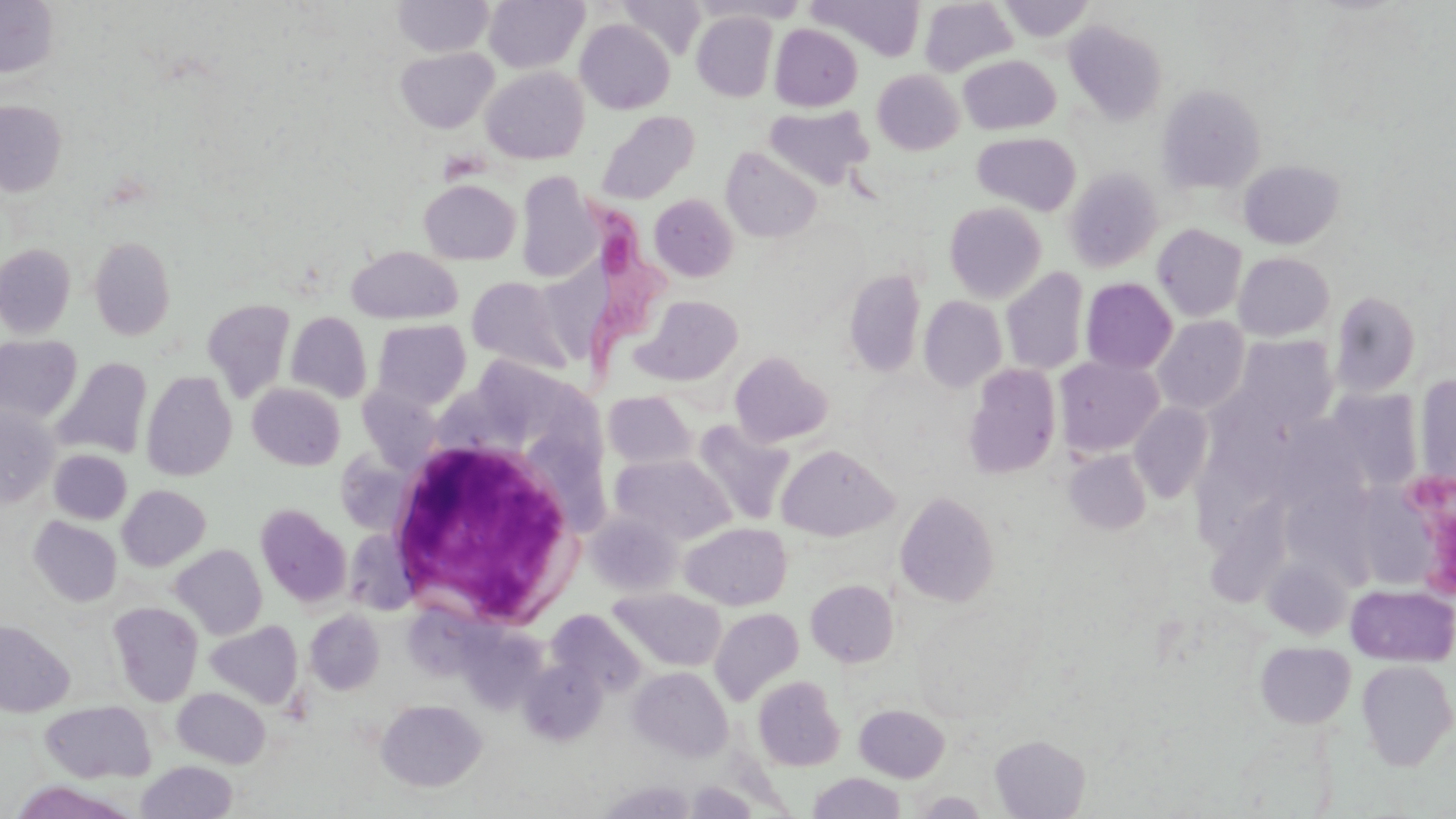
slide-level diagnosis = Trypanosoma brucei
field of view = one of a larger specimen
white blood cell locations = approximate bounding boxes as named x1/y1/x2/y2 corners in pixels: (x1=381, y1=428, x2=591, y2=628)
image size = 1456×819 pixels
modality = optical microscopy
Trypanosoma brucei locations = approximate bounding boxes as named x1/y1/x2/y2 corners in pixels: (x1=574, y1=194, x2=672, y2=372)
stain = May-Grünwald-Giemsa
magnification = 1000x
preparation = thin blood smear
uninfected red blood cell locations = approximate bounding boxes as named x1/y1/x2/y2 corners in pixels: (x1=392, y1=0, x2=495, y2=57), (x1=484, y1=0, x2=588, y2=74), (x1=616, y1=0, x2=707, y2=59), (x1=999, y1=0, x2=1093, y2=42), (x1=0, y1=1, x2=60, y2=79), (x1=919, y1=1, x2=1017, y2=75), (x1=692, y1=11, x2=778, y2=102), (x1=576, y1=19, x2=675, y2=114), (x1=1064, y1=20, x2=1167, y2=124), (x1=770, y1=23, x2=862, y2=111), (x1=395, y1=47, x2=498, y2=133), (x1=959, y1=56, x2=1060, y2=135), (x1=482, y1=66, x2=589, y2=164), (x1=872, y1=69, x2=963, y2=154), (x1=1156, y1=84, x2=1266, y2=194), (x1=0, y1=100, x2=66, y2=196), (x1=764, y1=105, x2=873, y2=189), (x1=595, y1=111, x2=699, y2=205), (x1=971, y1=132, x2=1081, y2=215), (x1=721, y1=147, x2=821, y2=243), (x1=1237, y1=160, x2=1345, y2=249), (x1=1064, y1=166, x2=1163, y2=272), (x1=515, y1=172, x2=600, y2=283), (x1=419, y1=179, x2=521, y2=265), (x1=649, y1=194, x2=738, y2=281), (x1=944, y1=201, x2=1047, y2=303), (x1=1152, y1=223, x2=1248, y2=322), (x1=89, y1=236, x2=175, y2=341), (x1=0, y1=244, x2=76, y2=338), (x1=346, y1=245, x2=462, y2=324), (x1=1234, y1=252, x2=1335, y2=341), (x1=1001, y1=266, x2=1090, y2=375), (x1=843, y1=268, x2=926, y2=377), (x1=467, y1=276, x2=573, y2=374), (x1=1080, y1=277, x2=1177, y2=374), (x1=1330, y1=291, x2=1421, y2=396), (x1=634, y1=295, x2=743, y2=386), (x1=918, y1=295, x2=1007, y2=393), (x1=201, y1=298, x2=296, y2=402), (x1=286, y1=311, x2=372, y2=404), (x1=1153, y1=316, x2=1250, y2=414), (x1=372, y1=319, x2=471, y2=408), (x1=0, y1=335, x2=82, y2=423), (x1=1232, y1=335, x2=1337, y2=431), (x1=729, y1=351, x2=833, y2=447), (x1=1055, y1=356, x2=1163, y2=457), (x1=54, y1=357, x2=152, y2=458), (x1=963, y1=364, x2=1062, y2=479), (x1=142, y1=370, x2=237, y2=481), (x1=1414, y1=374, x2=1456, y2=485), (x1=356, y1=382, x2=445, y2=472), (x1=248, y1=383, x2=345, y2=470), (x1=1323, y1=389, x2=1423, y2=492), (x1=603, y1=391, x2=697, y2=470), (x1=1129, y1=402, x2=1213, y2=502), (x1=0, y1=407, x2=60, y2=506), (x1=693, y1=421, x2=795, y2=526), (x1=775, y1=444, x2=898, y2=540), (x1=49, y1=449, x2=132, y2=524), (x1=1065, y1=449, x2=1152, y2=535), (x1=612, y1=454, x2=735, y2=545), (x1=1298, y1=466, x2=1400, y2=596), (x1=1377, y1=472, x2=1456, y2=596), (x1=117, y1=484, x2=210, y2=571), (x1=895, y1=490, x2=1000, y2=606), (x1=256, y1=504, x2=351, y2=607), (x1=1199, y1=505, x2=1300, y2=615), (x1=587, y1=512, x2=682, y2=597), (x1=28, y1=516, x2=122, y2=606), (x1=680, y1=522, x2=792, y2=610), (x1=170, y1=544, x2=267, y2=640), (x1=1263, y1=554, x2=1353, y2=639), (x1=806, y1=580, x2=899, y2=667), (x1=1346, y1=583, x2=1456, y2=667), (x1=609, y1=587, x2=727, y2=672), (x1=108, y1=602, x2=203, y2=706), (x1=709, y1=608, x2=804, y2=705), (x1=304, y1=610, x2=384, y2=694), (x1=548, y1=610, x2=646, y2=697), (x1=0, y1=619, x2=74, y2=717), (x1=205, y1=620, x2=303, y2=708), (x1=1255, y1=641, x2=1356, y2=729), (x1=520, y1=657, x2=606, y2=744), (x1=1356, y1=659, x2=1456, y2=770), (x1=630, y1=666, x2=732, y2=761), (x1=753, y1=675, x2=845, y2=771), (x1=173, y1=687, x2=271, y2=768), (x1=375, y1=699, x2=486, y2=792), (x1=40, y1=700, x2=155, y2=782), (x1=854, y1=704, x2=950, y2=782), (x1=990, y1=735, x2=1090, y2=818), (x1=137, y1=761, x2=238, y2=819), (x1=808, y1=772, x2=906, y2=818), (x1=11, y1=781, x2=142, y2=818), (x1=914, y1=791, x2=988, y2=818)